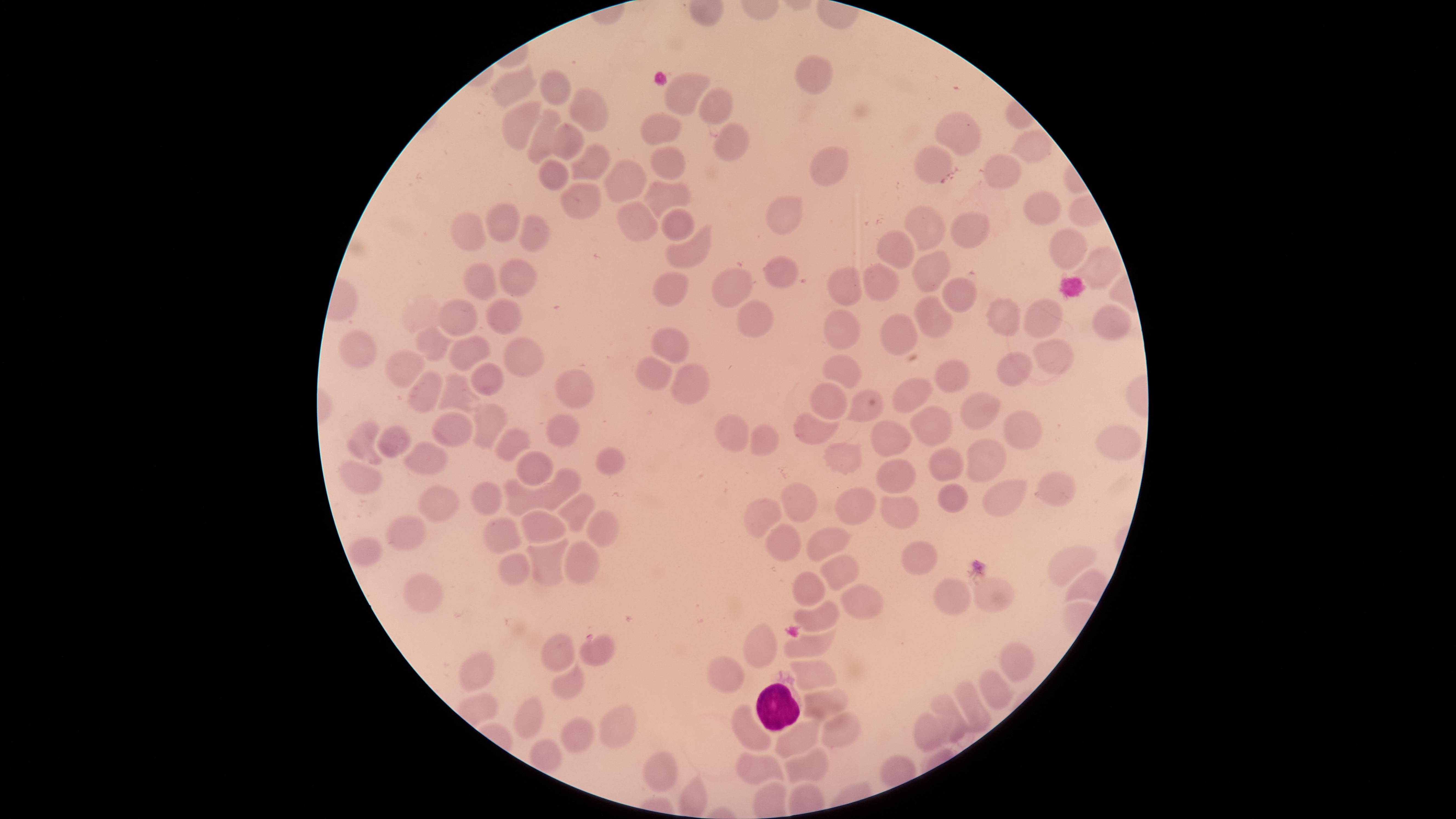

presence: malaria parasites detected
parasitized_red_blood_cells: 'approximate marker points as {x, y} in pixels: {596, 651}'
uninfected_red_blood_cells: 'approximate marker points as {x, y} in pixels: {816, 69}, {512, 90}, {555, 90}, {678, 96}, {718, 103}, {588, 108}, {515, 124}, {660, 131}, {964, 133}, {540, 140}, {571, 141}, {730, 141}, {1030, 146}, {669, 162}, {831, 164}, {596, 166}, {937, 166}, {1002, 173}, {627, 174}, {550, 183}, {665, 193}, {587, 201}, {1042, 206}, {783, 212}, {640, 221}, {677, 223}, {506, 227}, {928, 227}, {975, 233}, {476, 234}, {535, 237}, {902, 248}, {1062, 248}, {690, 251}, {1093, 265}, {781, 266}, {930, 271}, {514, 275}, {729, 285}, {668, 288}, {849, 289}, {883, 289}, {482, 291}, {956, 293}, {936, 313}, {1001, 315}, {454, 317}, {759, 318}, {501, 319}, {1043, 322}, {1111, 322}, {905, 335}, {845, 337}, {431, 343}, {359, 344}, {671, 345}, {470, 352}, {518, 354}, {1055, 356}, {844, 366}, {406, 370}, {1011, 373}, {948, 374}, {654, 377}, {693, 378}, {570, 380}, {484, 381}, {431, 389}, {911, 392}, {456, 395}, {832, 401}, {973, 406}, {865, 412}, {1008, 419}, {937, 426}, {488, 427}, {819, 427}, {556, 433}, {731, 433}, {452, 434}, {895, 435}, {765, 437}, {1114, 437}, {366, 439}, {393, 440}, {508, 442}, {422, 456}, {848, 456}, {981, 457}, {606, 461}, {943, 465}, {531, 472}, {896, 477}, {353, 481}, {554, 487}, {1055, 491}, {488, 493}, {514, 496}, {947, 498}, {1006, 500}, {801, 502}, {441, 505}, {569, 510}, {856, 510}, {894, 510}, {764, 515}, {601, 527}, {405, 531}, {500, 531}, {538, 533}, {827, 539}, {781, 541}, {922, 553}, {371, 555}, {579, 562}, {539, 564}, {1066, 568}, {513, 569}, {835, 573}, {422, 592}, {809, 592}, {947, 596}, {993, 597}, {859, 600}, {826, 614}, {817, 644}, {762, 646}, {556, 652}, {1014, 661}, {475, 672}, {813, 675}, {733, 680}, {565, 685}, {998, 685}, {970, 703}, {822, 705}, {525, 714}, {954, 718}, {614, 726}, {931, 728}, {835, 732}, {571, 735}, {754, 735}, {801, 739}, {655, 764}, {767, 768}, {811, 768}'
species: Plasmodium falciparum
capture: smartphone photograph through the microscope eyepiece
field_of_view: single
white_blood_cells: 'approximate marker points as {x, y} in pixels: {775, 707}'
image_size: 1456×819 pixels
visible_region: circular
preparation: thin blood smear
stain: Giemsa